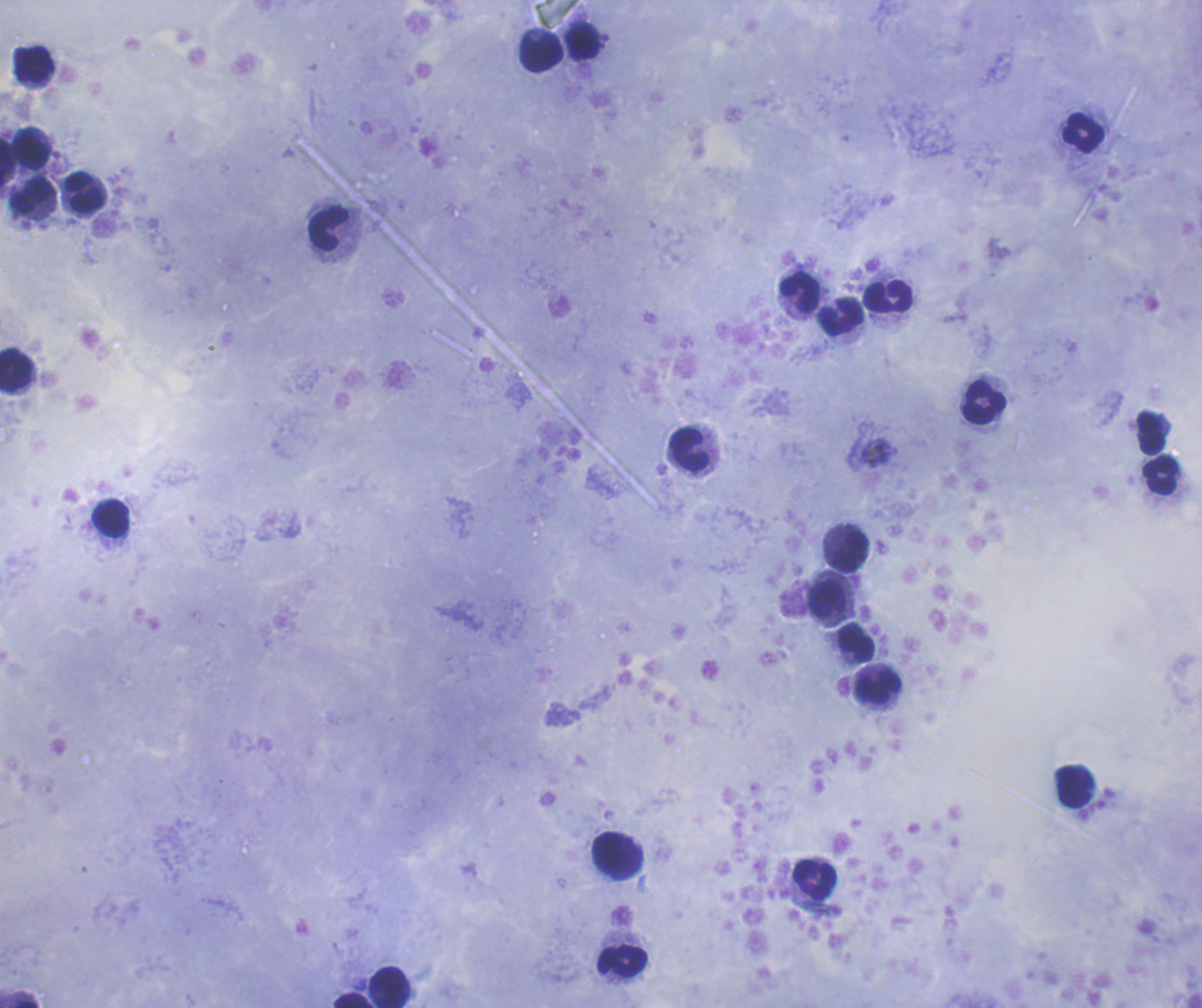

Approximate object centers, in pixels from the top-left corner.
Summary:
  - Leukocyte locations: (x=583, y=42), (x=543, y=54), (x=34, y=64), (x=1083, y=132), (x=33, y=150), (x=7, y=160), (x=84, y=192), (x=31, y=196), (x=329, y=228), (x=800, y=293), (x=888, y=296), (x=841, y=316), (x=16, y=370), (x=984, y=402), (x=1152, y=433), (x=690, y=450), (x=1160, y=475), (x=110, y=518), (x=851, y=551), (x=828, y=598), (x=856, y=642), (x=878, y=688), (x=1075, y=787), (x=618, y=856), (x=815, y=879), (x=622, y=960), (x=390, y=987), (x=352, y=1000)
  - Magnification: 100x
  - Context: previously used in an actual diagnosis
  - Stain: Romanowsky
  - Background quality: good
  - Preparation: thick blood film
  - Image size: 1202×1008 pixels
  - Field of view: single
  - Coloration quality: good
  - Result: no Plasmodium parasites seen